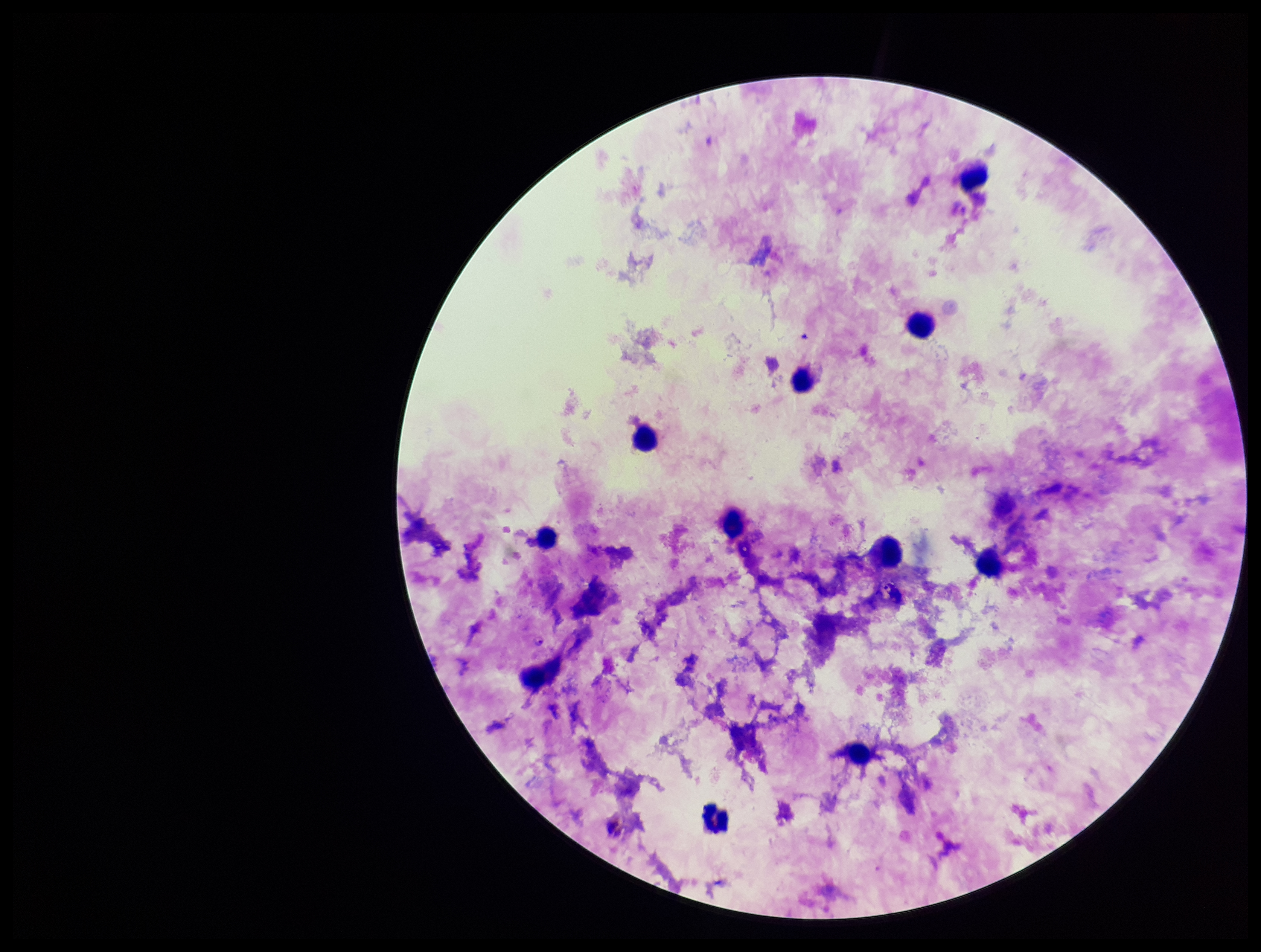
Summary:
  - Field of view: one from this slide
  - Plasmodium parasites: identified
  - Species reported for this patient: Plasmodium falciparum
  - Leukocyte count: 14
  - Stain: Giemsa
  - Image size: 1261×952 pixels
  - Capture: smartphone photograph through the microscope eyepiece
  - Preparation: thick smear
  - Parasite count: 1
  - Patient malaria status: infected